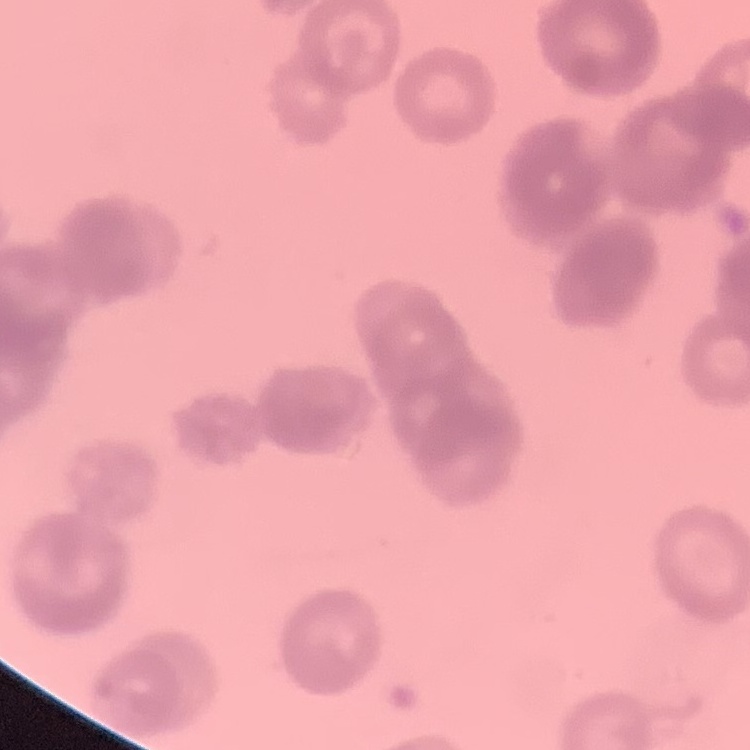
Summary:
  - Erythrocyte morphology: rouleaux formation
  - Image type: one tile cut from a larger photomicrograph
  - Preparation: thin blood film
  - Stain: Field's or Giemsa